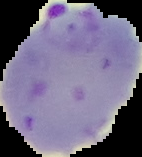

Summary:
  - Preparation: thin blood smear
  - Malaria status: parasitized
  - Image type: segmented cell region on a black background
  - Image size: 142×157 pixels